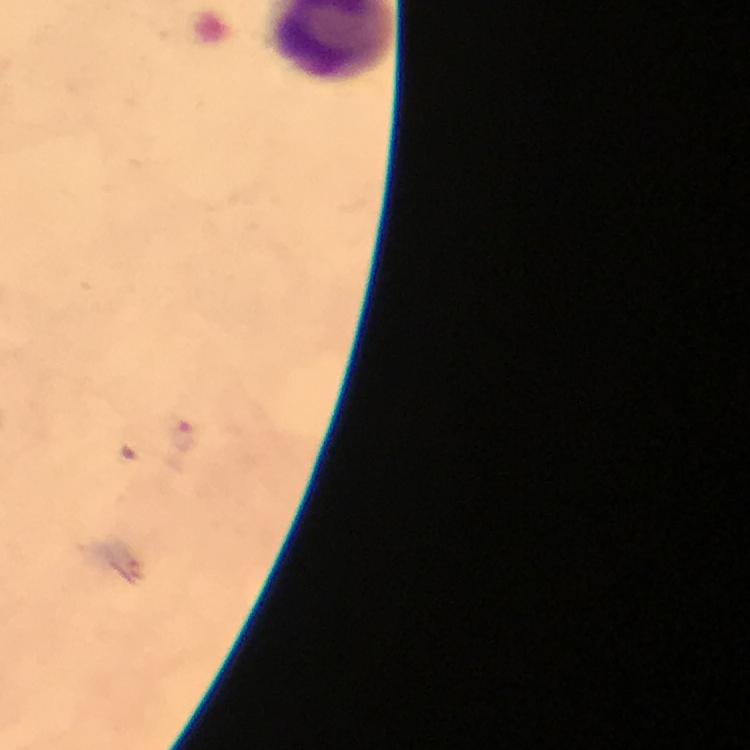

Approximate centers as (x, y) in pixels.
Summary:
  - Malaria parasite locations: (186, 438), (128, 452)
  - Image size: 750×750 pixels
  - Stain: Giemsa
  - Context: from a diagnostic examination for malaria
  - Cropped from: one field of view
  - Immersion oil: used
  - Magnification: 100x
  - Preparation: thick blood film
  - Capture: smartphone photograph through a microscope